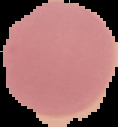

image type = segmented cell region with the area outside set to black
image size = 118×127 pixels
preparation = thin blood film
malaria status = uninfected